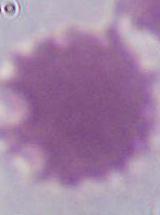

Summary:
  - Modality: photomicrograph
  - Identification: red blood cell
  - Magnification: 1000x